Assess this cell for malaria.
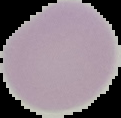

Uninfected.

From a thin blood smear. The area outside the segmented cell region is set to black. Image is 121×118 pixels.